State which parasite is depicted.
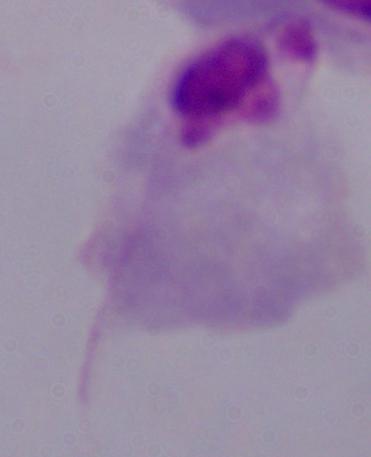

A trichomonad.

Micrograph. Captured at 1000x magnification.